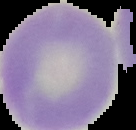
preparation = thin blood smear
malaria status = uninfected
image type = cell region segmented out of the field of view; surrounding area masked to black
image size = 136×130 pixels